Locate every blood parasite and identify its species.
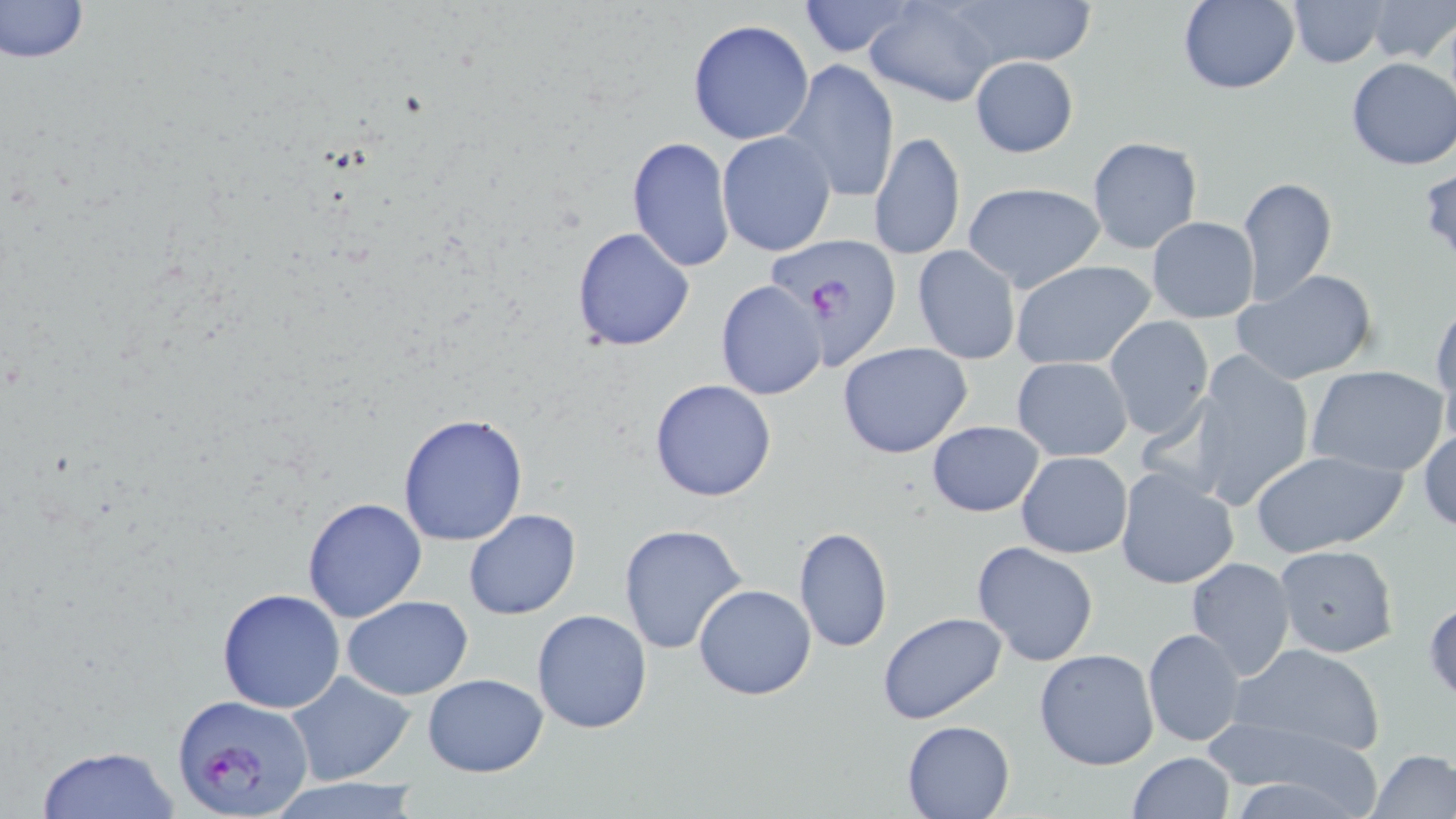

Approximate bounding boxes as (x1,y1)-(x2,y2) corner pairs in pixels.
Plasmodium falciparum-infected red blood cells: (767,235)-(904,367), (169,694)-(314,817).
No Plasmodium ovale, Plasmodium malariae, Plasmodium vivax, Babesia divergens, or Trypanosoma brucei observed.

Summary:
  - Uninfected red blood cell locations: (0,0)-(92,65), (794,0)-(919,58), (941,0)-(1097,70), (1175,0)-(1300,96), (1368,0)-(1456,63), (864,1)-(1000,107), (1289,2)-(1387,68), (688,19)-(815,144), (970,56)-(1078,157), (1345,58)-(1456,171), (781,59)-(899,204), (869,131)-(966,262), (717,132)-(836,256), (1086,135)-(1202,253), (626,137)-(736,272), (1416,166)-(1456,266), (1237,176)-(1338,305), (961,182)-(1107,292), (1147,217)-(1259,323), (572,226)-(694,351), (912,245)-(1020,363), (1011,259)-(1156,369), (1229,268)-(1379,386), (714,280)-(828,400), (1430,297)-(1456,424), (1103,316)-(1214,440), (837,343)-(974,459), (1189,351)-(1316,512), (1011,357)-(1133,460), (1305,365)-(1451,479), (649,379)-(778,502), (398,412)-(528,546), (927,420)-(1044,517), (1417,426)-(1456,533), (1251,448)-(1406,557), (1016,451)-(1133,559), (1114,466)-(1238,591), (301,496)-(428,624), (463,508)-(581,620), (618,523)-(749,655), (794,525)-(892,653), (971,541)-(1099,667), (1273,544)-(1400,658), (1185,556)-(1297,680), (694,584)-(817,700), (216,588)-(346,713), (342,595)-(474,700), (531,609)-(652,734), (877,611)-(1007,726), (1142,627)-(1247,748), (1225,641)-(1386,760), (1034,648)-(1161,771), (286,670)-(417,784), (422,672)-(550,777), (902,719)-(1017,818), (1216,733)-(1383,815), (33,745)-(182,819), (1367,748)-(1456,818), (1126,751)-(1234,819), (265,777)-(428,819)
  - Slide-level diagnosis: Plasmodium falciparum
  - Magnification: 1000x
  - Field of view: one of a larger specimen
  - Preparation: thin blood film
  - Modality: optical microscopy
  - Stain: May-Grünwald-Giemsa
  - Image size: 1456×819 pixels